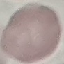
result = no malaria parasites detected
stain = Giemsa
preparation = thin blood film
image type = automatically extracted cell patch, resized to 64 × 64 pixels
capture = smartphone camera at the microscope eyepiece